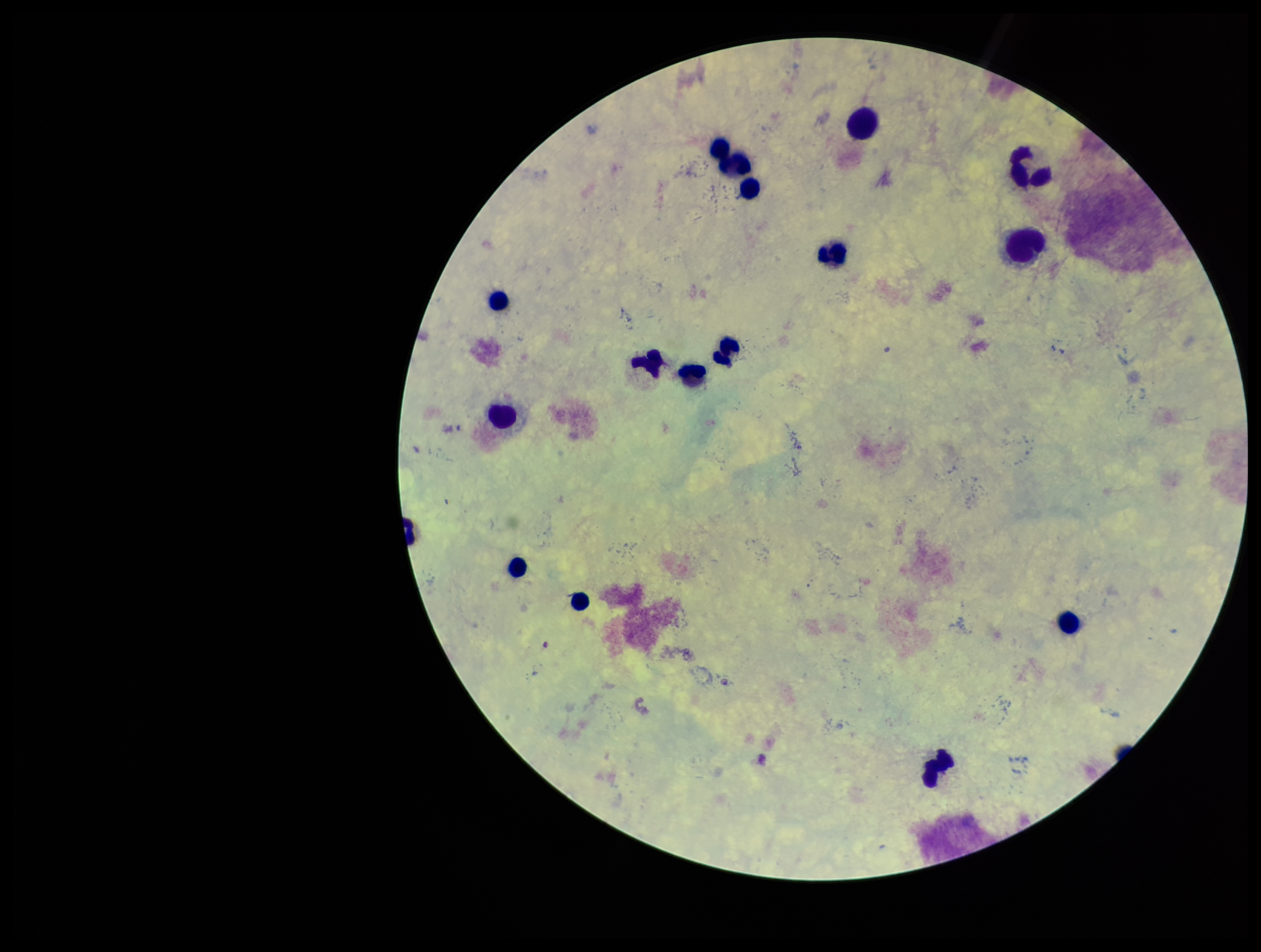

Summary:
  - Preparation: thick
  - Patient malaria status: negative
  - Image size: 1261×952 pixels
  - Leukocyte count: 16
  - Field of view: one from this slide
  - Plasmodium parasites: none detected
  - Stain: Giemsa
  - Capture: smartphone photograph through the microscope eyepiece
  - Parasite count: 0